Locate every P. falciparum parasite and identify its life-cycle stage.
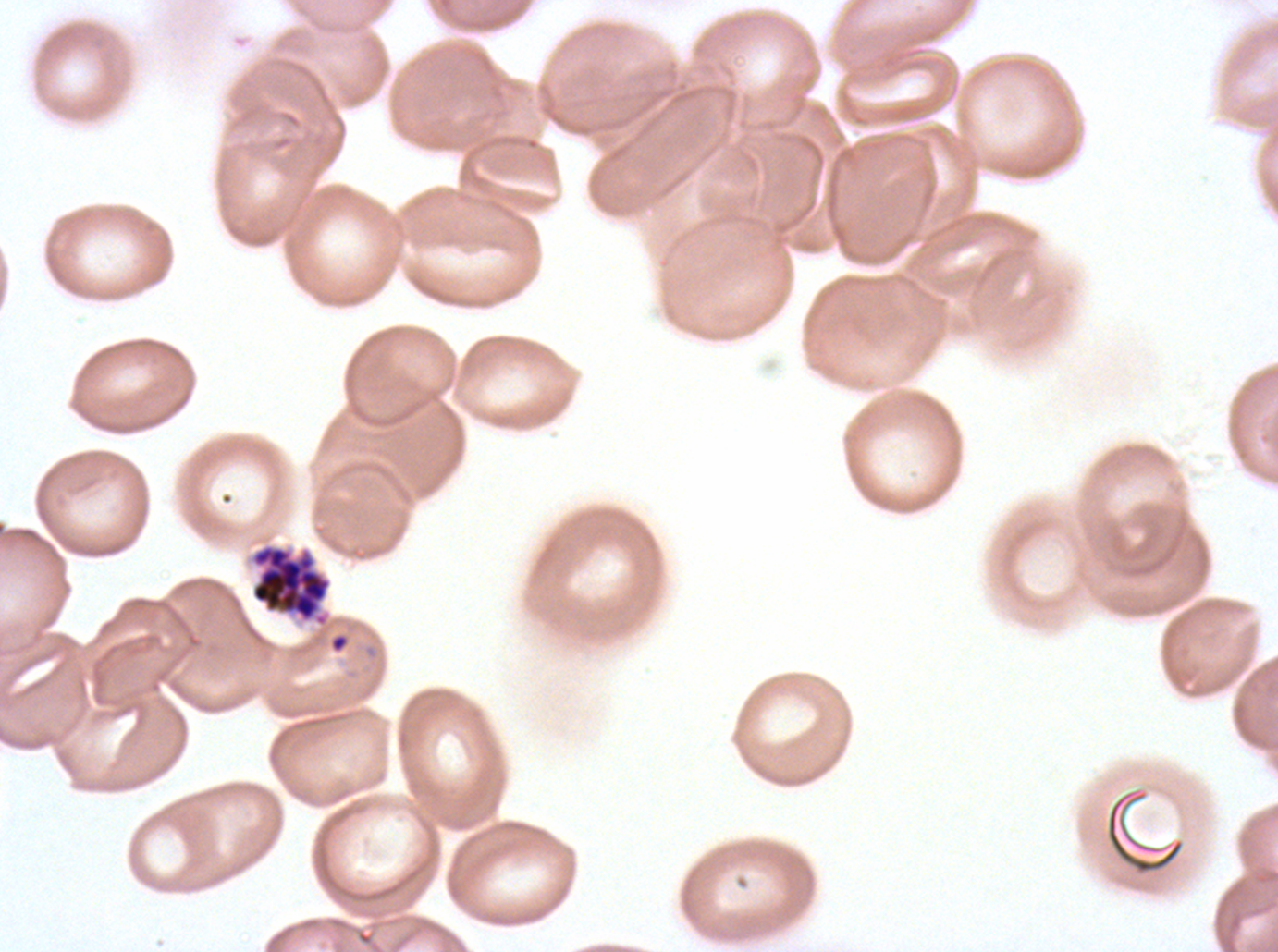
Approximate bounding rectangles given as corner coordinates in pixels from the top-left.
Rings: (x1=328, y1=632, x2=350, y2=654).
Segmenters: (x1=249, y1=543, x2=332, y2=628).
No late-ring/early-trophozoite forms, mid trophozoites, late trophozoites, early schizonts, late schizonts, or gametocytes observed.

{
  "field_of_view": "sub-image separated from a larger composite",
  "life_cycle_stages_observed": "ring, segmenter",
  "image_size": "1278×952 pixels",
  "stain": "Giemsa",
  "preparation": "thin blood smear",
  "specimen": "P. falciparum from a patient in The Gambia, cultured ex vivo for 24 to 48 hours",
  "debris_locations": "approximate bounding rectangles given as corner coordinates in pixels from the top-left: (x1=1105, y1=787, x2=1186, y2=876)"
}